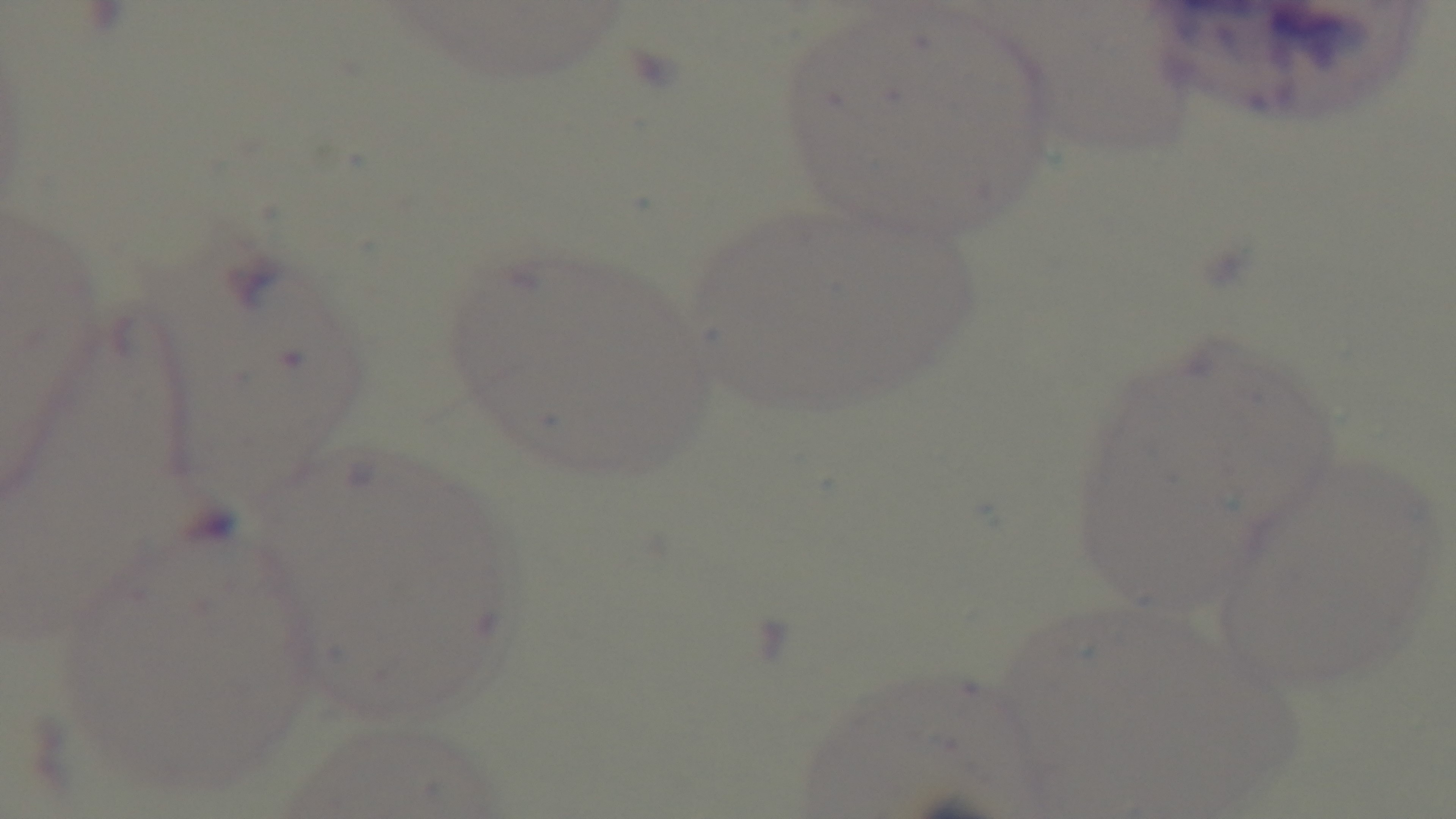 Single field of view. Photomicrograph. Giemsa stain. Preparation: thin blood film. Malaria status: uninfected. Mounted 4K digital camera. Oil-immersion objective, 100x.